Describe the morphology of the erythrocytes.
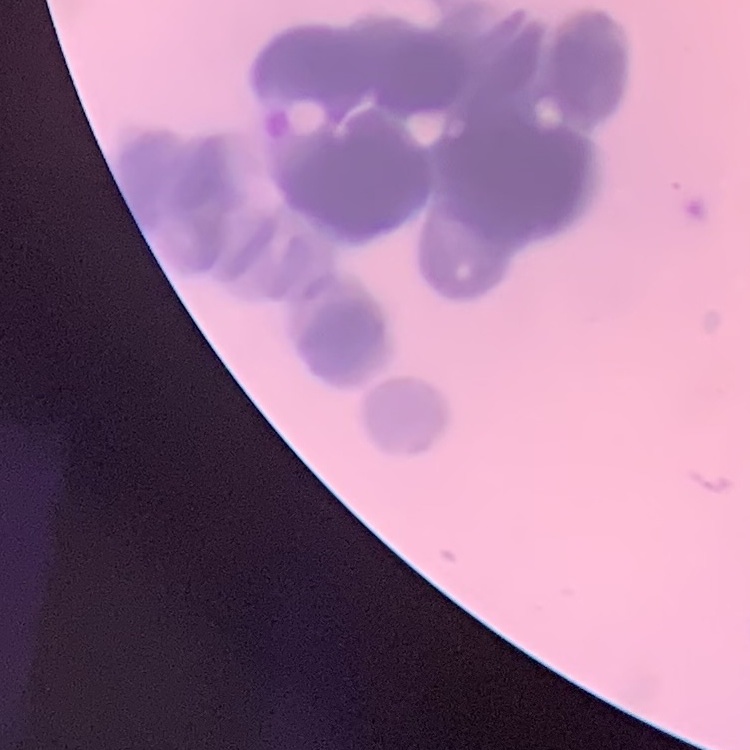
They show rouleaux formation.

Thin blood smear. One tile cut from a larger photomicrograph. Stained with either Field's or Giemsa.